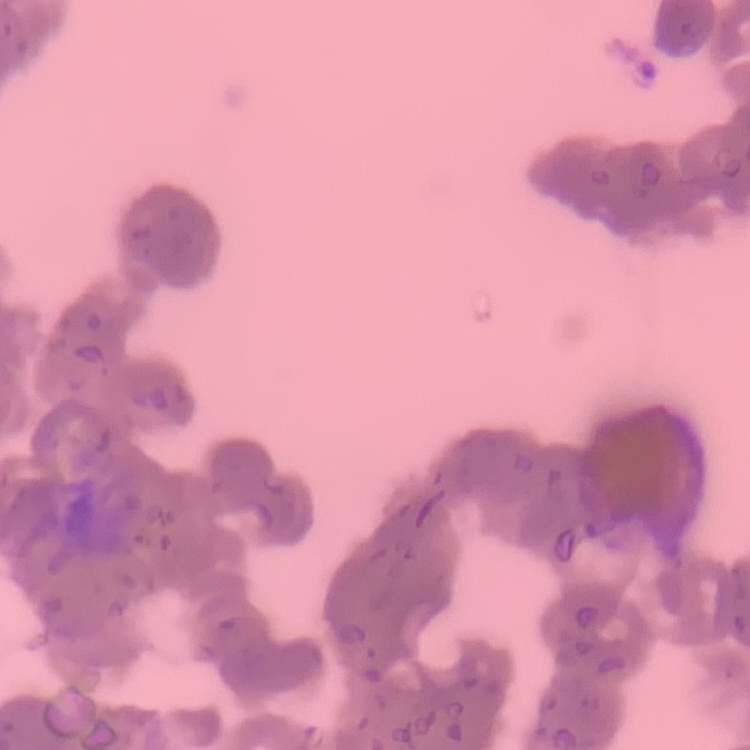
red blood cell morphology = rouleaux formation
stain = Field's or Giemsa
image type = one tile cut from a larger photomicrograph
preparation = thin blood smear